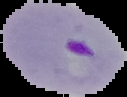

Summary:
  - Preparation: thin blood film
  - Result: Plasmodium parasites detected
  - Image size: 127×97 pixels
  - Image type: segmented cell region on a black background